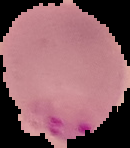 From a thin blood film. Segmented cell region on a black background. Malaria status: parasitized. Image is 130×148 pixels.